Comment on the morphology of the red blood cells.
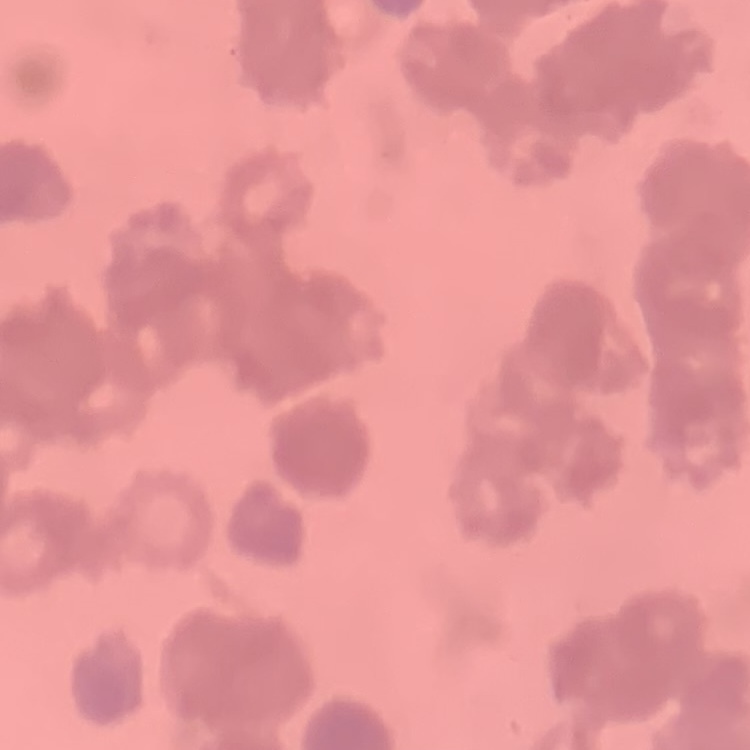
They show rouleaux formation.

preparation = thin peripheral smear
stain = Field's or Giemsa
image type = square crop of a larger photomicrograph